Comment on the morphology of the erythrocytes.
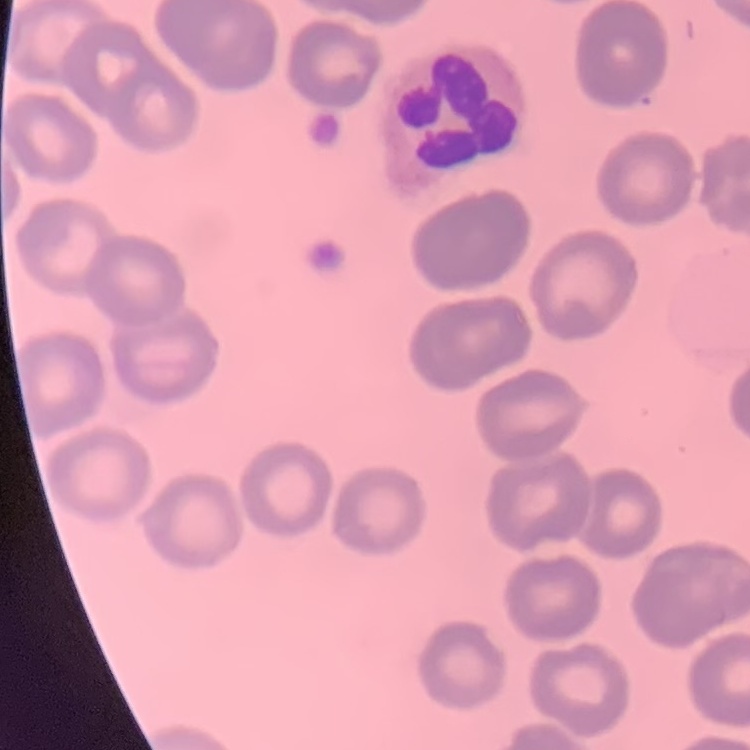
They show no rouleaux formation.

Field's or Giemsa stain. Thin peripheral smear. One tile cut from a larger photomicrograph.